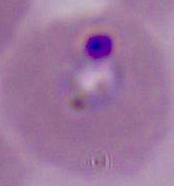 Micrograph. Captured at either 400x or 1000x magnification. A Plasmodium parasite is seen.